Locate every blood parasite and identify its species.
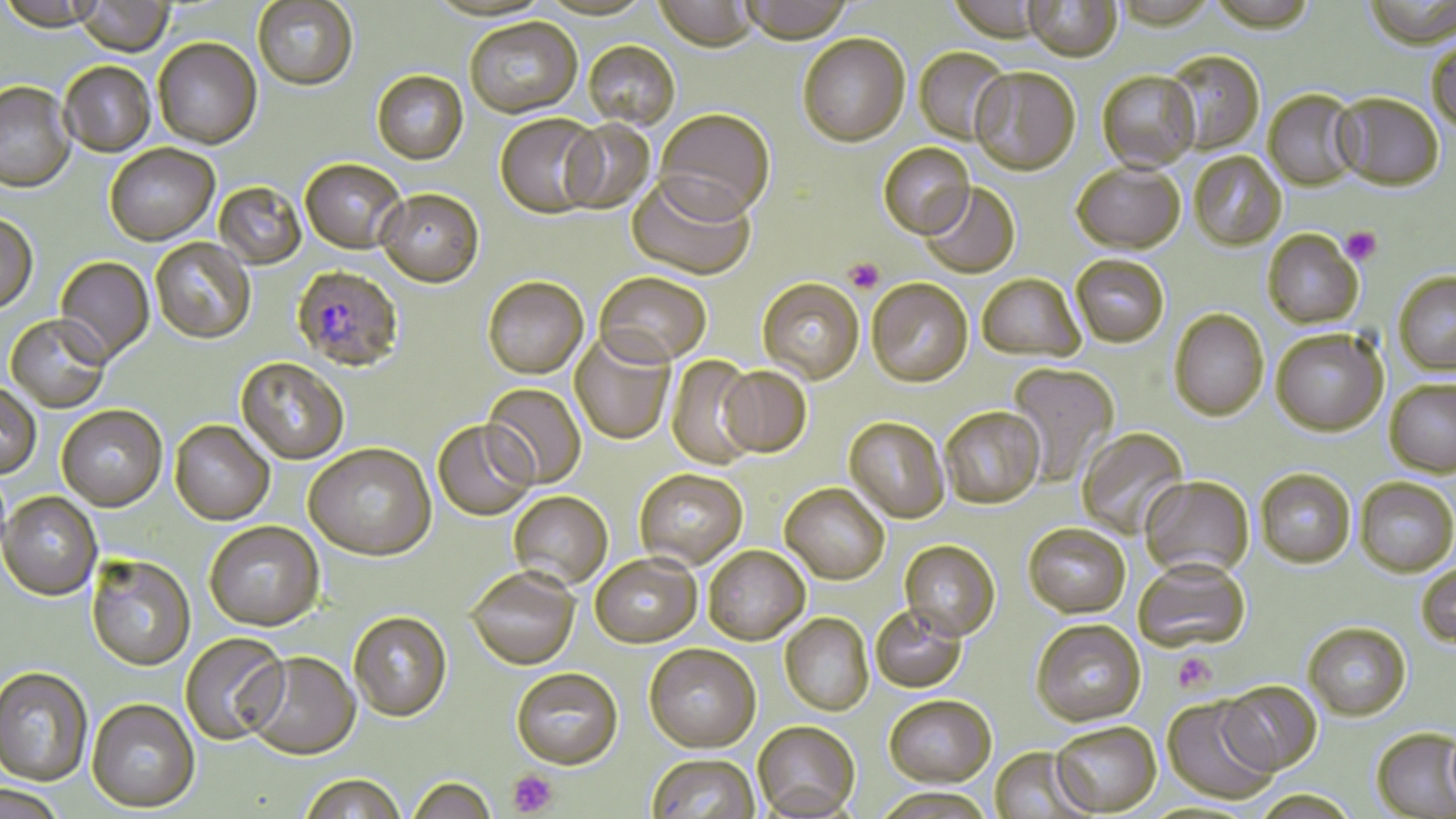
Approximate bounding boxes as (x1, y1, x2, y2) in pixels.
Plasmodium falciparum-infected red blood cells: (292, 267, 404, 374).
No Plasmodium ovale, Plasmodium malariae, Plasmodium vivax, Babesia divergens, or Trypanosoma brucei observed.

slide_level_diagnosis: Plasmodium falciparum
modality: optical microscopy
platelet_locations: 'approximate bounding boxes as (x1, y1, x2, y2) in pixels: (1341, 226, 1381, 264), (845, 258, 884, 294), (1172, 653, 1215, 694), (507, 770, 559, 817)'
image_size: 1456×819 pixels
magnification: 1000x
stain: May-Grünwald-Giemsa
uninfected_red_blood_cell_locations: 'approximate bounding boxes as (x1, y1, x2, y2) in pixels: (253, 0, 358, 92), (426, 0, 554, 24), (539, 0, 656, 23), (655, 0, 757, 55), (739, 0, 855, 46), (947, 0, 1047, 46), (1207, 0, 1318, 34), (1364, 0, 1456, 50), (0, 1, 106, 35), (74, 1, 175, 59), (1024, 1, 1122, 64), (465, 20, 582, 120), (798, 37, 910, 150), (153, 39, 262, 152), (1427, 40, 1456, 136), (583, 43, 679, 131), (914, 48, 1010, 146), (1163, 52, 1265, 155), (60, 63, 155, 159), (970, 69, 1081, 178), (372, 71, 469, 166), (1097, 73, 1200, 174), (0, 83, 76, 195), (1264, 91, 1361, 192), (1333, 94, 1444, 191), (654, 111, 775, 226), (495, 116, 603, 221), (560, 120, 656, 215), (878, 145, 975, 242), (105, 146, 220, 247), (1189, 153, 1286, 252), (300, 161, 407, 256), (1072, 165, 1185, 257), (626, 178, 754, 283), (214, 183, 306, 271), (920, 184, 1021, 280), (376, 191, 484, 291), (0, 216, 38, 316), (1262, 231, 1363, 330), (150, 239, 256, 346), (54, 257, 155, 368), (1071, 257, 1169, 350), (1394, 273, 1456, 377), (594, 274, 711, 370), (977, 276, 1085, 364), (482, 280, 588, 382), (757, 280, 864, 386), (867, 280, 973, 390), (1169, 311, 1269, 423), (5, 317, 110, 414), (1271, 331, 1387, 438), (569, 334, 676, 445), (664, 356, 762, 471), (235, 359, 349, 466), (1006, 364, 1119, 488), (717, 368, 812, 460), (1385, 382, 1456, 478), (481, 383, 586, 490), (0, 384, 41, 480), (56, 407, 168, 513), (940, 409, 1045, 511), (844, 419, 949, 525), (169, 422, 274, 526), (432, 422, 535, 522), (1077, 428, 1190, 539), (304, 446, 437, 563), (1256, 471, 1355, 570), (635, 472, 748, 572), (1140, 478, 1255, 582), (1355, 480, 1456, 579), (780, 486, 889, 587), (0, 493, 102, 602), (508, 493, 612, 592), (205, 523, 324, 634), (1023, 526, 1130, 621), (899, 542, 1001, 644), (703, 548, 810, 647), (86, 557, 196, 673), (591, 557, 702, 651), (1134, 564, 1251, 656), (1417, 564, 1456, 649), (466, 571, 580, 673), (870, 607, 968, 695), (349, 614, 453, 724), (780, 614, 874, 717), (1031, 623, 1146, 730), (1303, 626, 1411, 724), (180, 634, 288, 747), (644, 646, 761, 756), (244, 653, 361, 762), (0, 668, 93, 787), (512, 670, 623, 773), (1218, 683, 1322, 777), (883, 698, 997, 791), (1161, 698, 1277, 806), (86, 700, 201, 814), (752, 723, 860, 819), (1051, 725, 1161, 817), (1371, 730, 1456, 818), (988, 749, 1092, 818), (647, 757, 759, 819), (299, 777, 406, 819), (407, 779, 496, 819), (2, 787, 65, 819), (872, 791, 997, 819), (1252, 793, 1360, 819)'
field_of_view: single
preparation: thin blood film